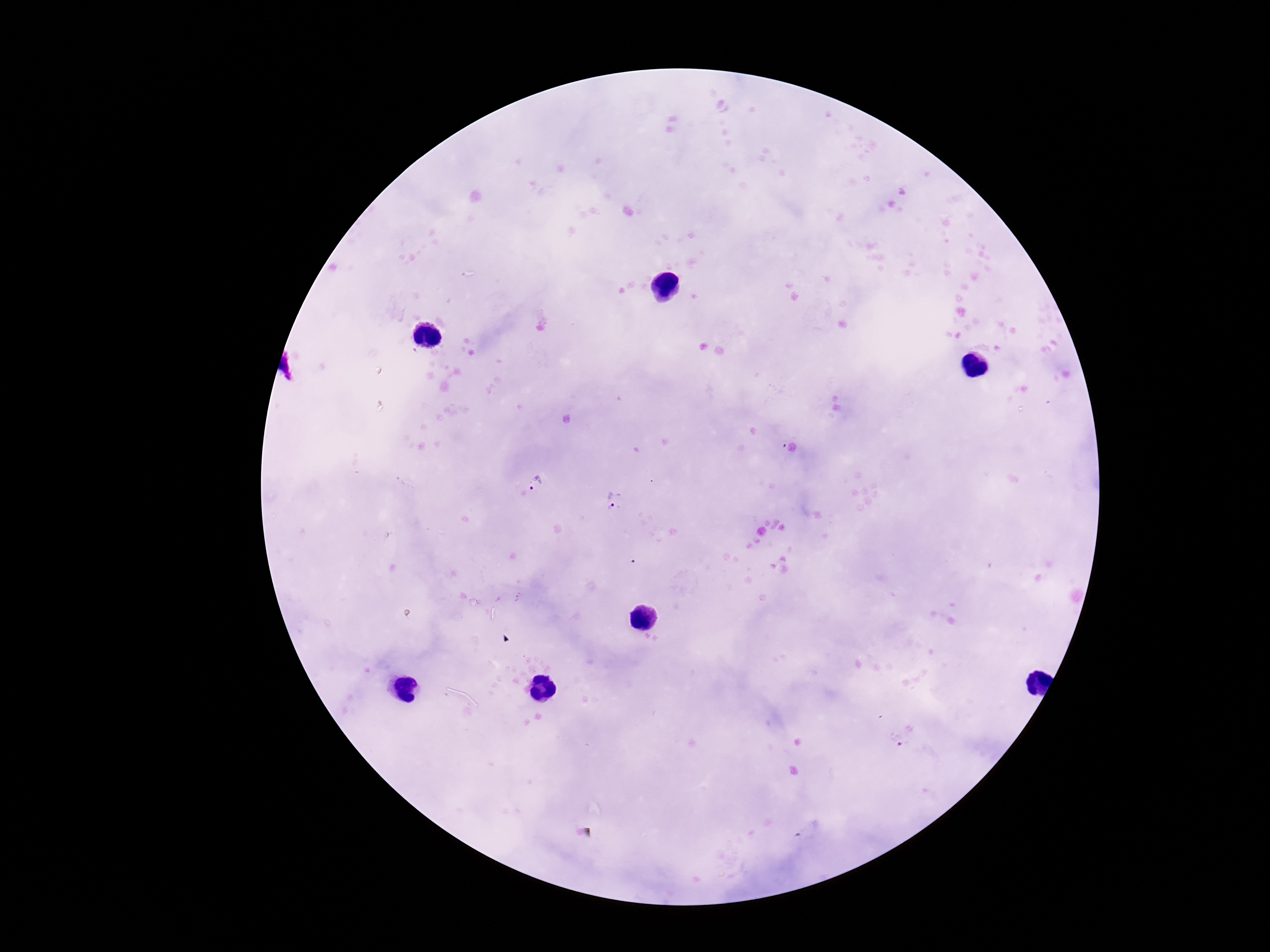

Approximate object centers, in pixels from the top-left corner. Plasmodium parasite locations: (x=536, y=484), (x=613, y=500), (x=898, y=740), (x=807, y=831). Single field of view. Giemsa stain. Thick blood film. Image is 1270×952 pixels. 100x magnification. Patient malaria status: infected. Photographed through the microscope eyepiece with a smartphone camera.